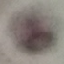

Result: no malaria parasites seen. Thin blood smear. Giemsa-stained preparation. Photographed with a smartphone camera at the microscope eyepiece. Automatically extracted cell patch, resized to 64 × 64 pixels.